Report the malaria status of this cell.
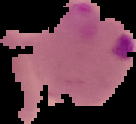
Parasitized.

image size = 136×124 pixels
preparation = thin blood smear
image type = cell region segmented out of the field of view; surrounding area masked to black